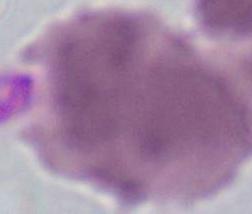
Summary:
  - Modality: micrograph
  - Identification: red blood cell
  - Magnification: 1000x